Identify the parasite.
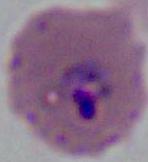
Plasmodium.

Micrograph. Captured at either 400x or 1000x magnification.